Name the blood parasite species.
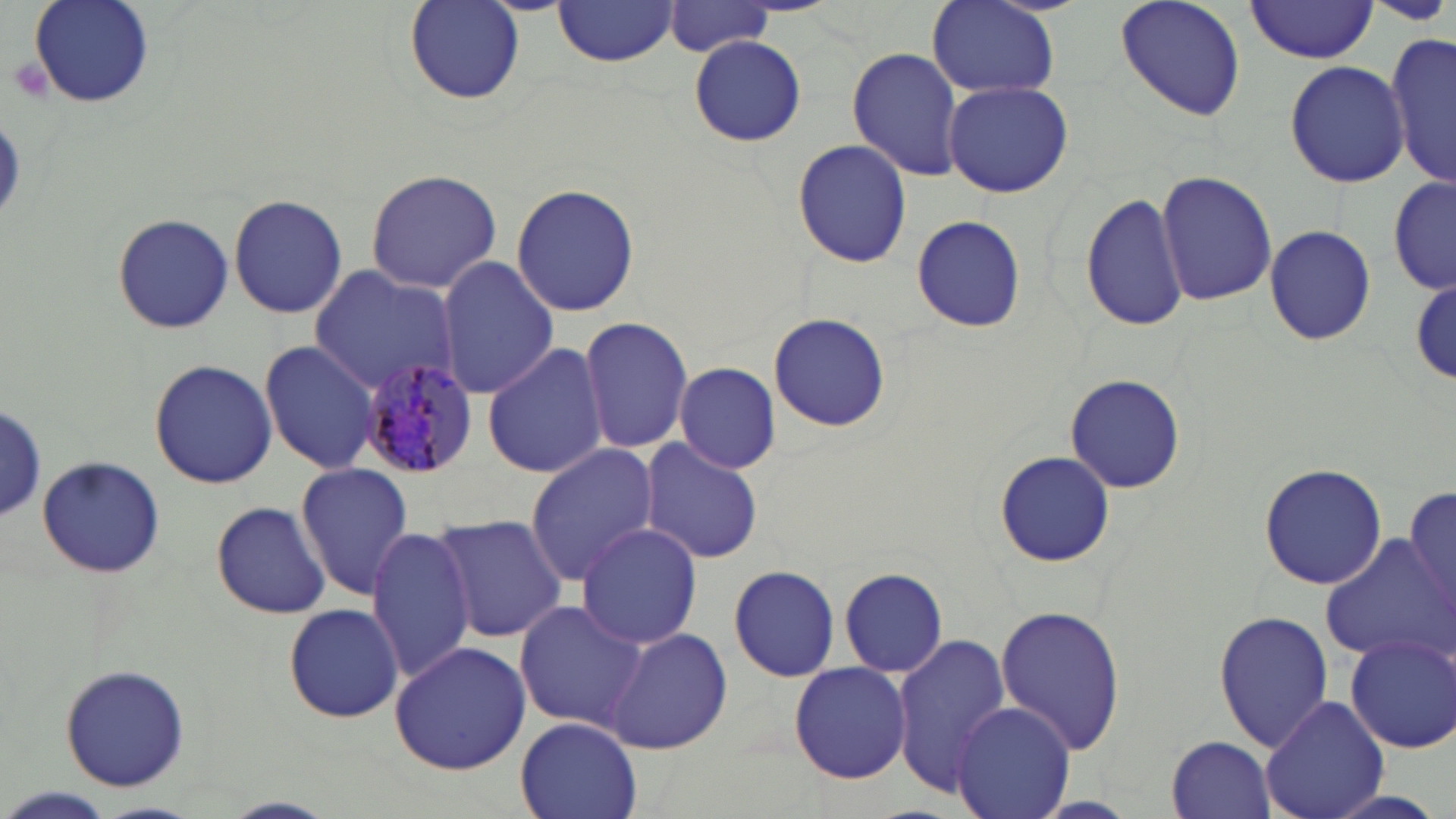
Plasmodium malariae.

Summary:
  - Coordinate format: approximate bounding boxes as (x1,y1)-(x2,y2) corner pairs in pixels
  - Plasmodium malariae-infected red blood cell locations: (356,357)-(480,479)
  - Platelet locations: (7,57)-(53,103)
  - Uninfected red blood cell locations: (405,0)-(526,104), (1114,0)-(1246,120), (29,1)-(156,109), (552,1)-(680,68), (926,1)-(1059,97), (1245,2)-(1380,63), (661,3)-(778,56), (1387,30)-(1456,189), (690,36)-(807,146), (846,48)-(963,181), (1285,59)-(1409,187), (943,80)-(1073,198), (792,140)-(914,267), (362,168)-(504,296), (1155,169)-(1275,305), (1389,175)-(1456,295), (509,182)-(643,320), (1081,190)-(1193,332), (227,194)-(347,320), (111,211)-(233,332), (910,216)-(1026,332), (1261,223)-(1378,347), (436,257)-(559,399), (306,266)-(463,395), (1411,276)-(1455,385), (768,313)-(891,433), (579,315)-(694,454), (259,341)-(379,472), (483,342)-(607,480), (150,357)-(276,488), (674,362)-(784,473), (1064,375)-(1188,494), (0,404)-(46,524), (639,439)-(764,568), (524,444)-(661,583), (994,450)-(1115,569), (35,457)-(165,578), (1258,462)-(1388,590), (296,463)-(413,599), (1403,481)-(1456,622), (210,500)-(333,619), (432,514)-(565,644), (575,522)-(702,648), (367,526)-(476,685), (1320,535)-(1456,662), (725,564)-(842,682), (840,568)-(949,677), (513,601)-(647,731), (283,604)-(405,723), (994,604)-(1127,758), (1213,607)-(1333,753), (606,627)-(732,755), (1343,631)-(1456,753), (892,634)-(1015,793), (389,641)-(530,775), (59,662)-(191,793), (790,663)-(912,784), (1261,695)-(1389,819), (951,700)-(1076,819), (515,718)-(641,818), (1167,735)-(1277,817), (5,788)-(115,819)
  - Stain: May-Grünwald-Giemsa
  - Modality: light microscopy
  - Image size: 1456×819 pixels
  - Preparation: thin blood smear
  - Magnification: 1000x
  - Field of view: single